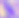

Summary:
  - Modality: micrograph
  - Magnification: 400x
  - Identification: Toxoplasma gondii